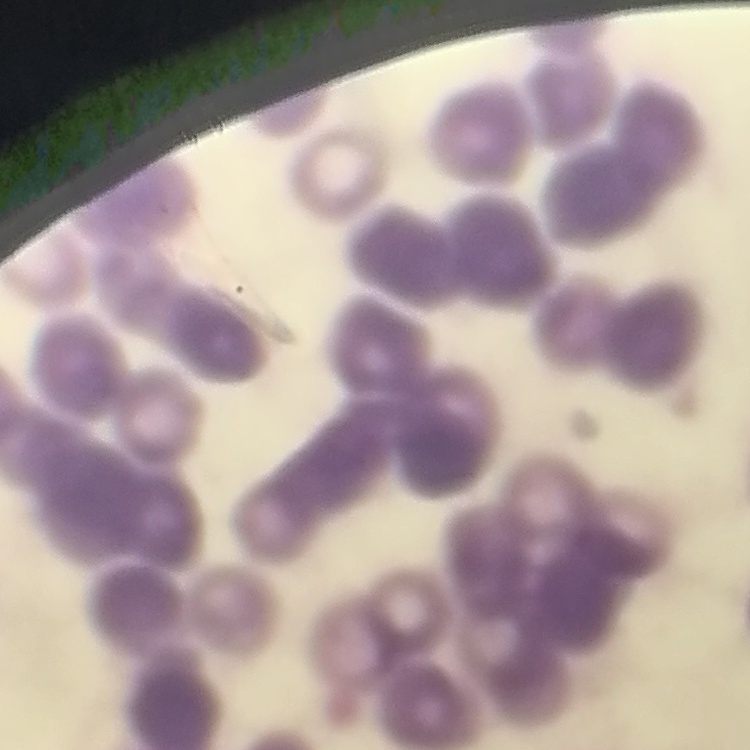
erythrocyte morphology = rouleaux formation
stain = Field's or Giemsa
preparation = thin blood film
image type = one tile cut from a larger photomicrograph